Classify this cell by malaria status.
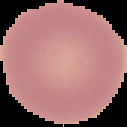
It is uninfected.

Summary:
  - Image size: 127×127 pixels
  - Preparation: thin blood film
  - Image type: cell region segmented out of the field of view; surrounding area masked to black